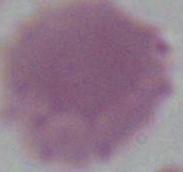

Summary:
  - Magnification: 1000x
  - Identification: red blood cell
  - Modality: micrograph